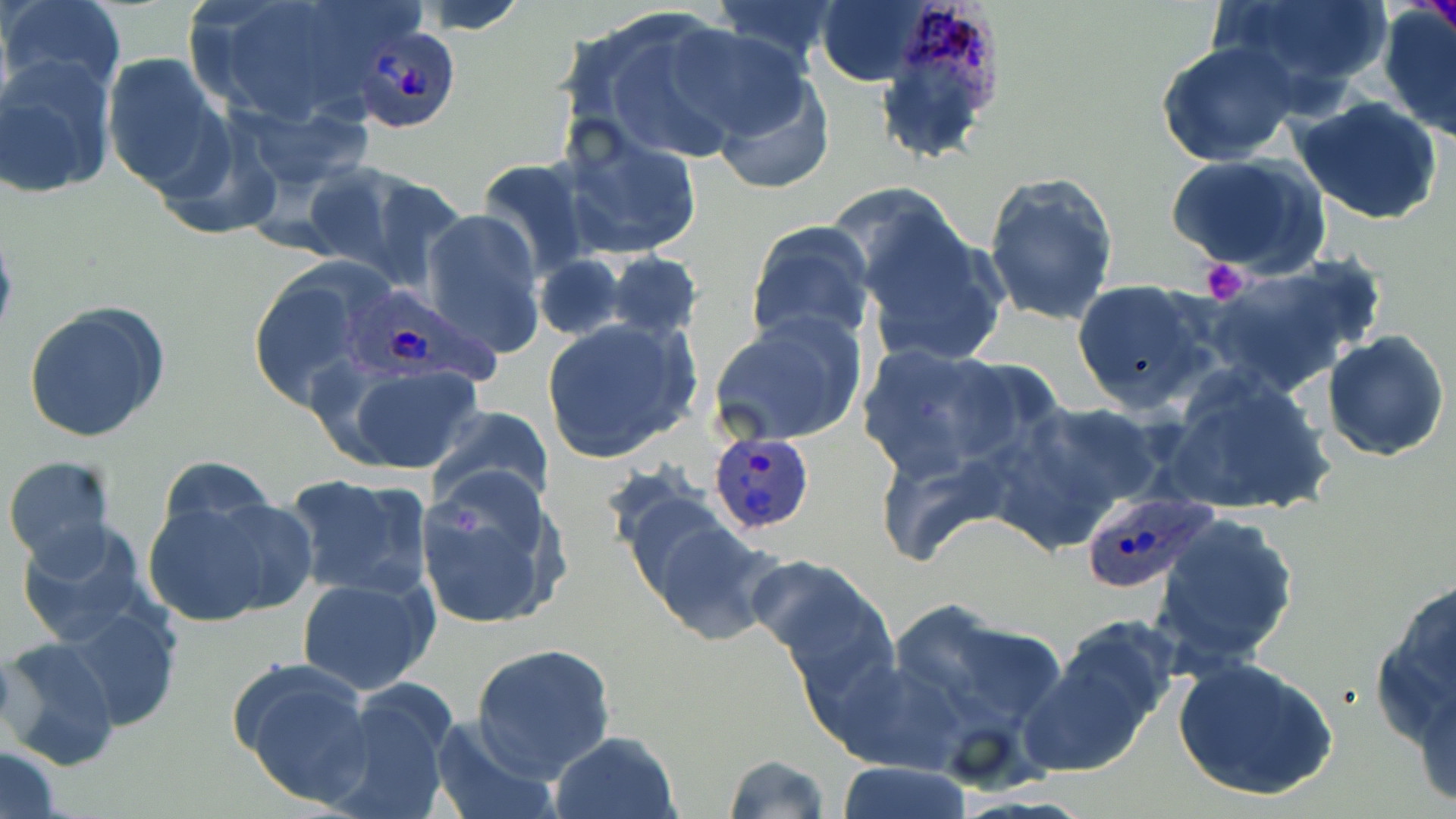

Approximate bounding boxes as (x1, y1, x2, y2) in pixels. Uninfected red blood cell locations: (1, 0, 126, 101), (186, 0, 409, 130), (410, 0, 532, 35), (705, 0, 848, 72), (815, 0, 931, 86), (1207, 0, 1396, 110), (1379, 4, 1456, 137), (570, 10, 750, 164), (663, 23, 819, 147), (1156, 42, 1299, 168), (101, 53, 231, 199), (1, 57, 117, 201), (710, 69, 835, 195), (1290, 95, 1444, 225), (562, 126, 703, 261), (1166, 153, 1327, 279), (475, 160, 596, 282), (303, 162, 457, 288), (982, 171, 1120, 328), (848, 198, 1010, 368), (420, 208, 546, 360), (745, 221, 876, 349), (605, 253, 702, 340), (534, 254, 625, 341), (1199, 254, 1386, 398), (244, 260, 395, 415), (1070, 279, 1219, 415), (22, 301, 170, 444), (709, 313, 870, 445), (542, 316, 701, 464), (1321, 331, 1452, 461), (854, 343, 1022, 480), (334, 361, 487, 476), (1160, 366, 1336, 517), (1013, 401, 1169, 522), (425, 405, 551, 513), (872, 443, 1010, 569), (2, 454, 118, 570), (159, 458, 276, 536), (413, 465, 564, 632), (283, 473, 435, 602), (141, 490, 313, 627), (631, 506, 787, 647), (1151, 511, 1300, 671), (16, 521, 153, 651), (753, 554, 903, 697), (296, 574, 440, 696), (1367, 579, 1456, 750), (896, 602, 1069, 732), (59, 603, 183, 731), (1031, 621, 1176, 769), (3, 637, 123, 770), (471, 643, 617, 780), (1172, 656, 1339, 803), (229, 658, 375, 810), (822, 658, 962, 774), (321, 682, 460, 819), (1411, 684, 1456, 809), (429, 713, 558, 819), (546, 731, 681, 819), (1, 746, 62, 818), (720, 753, 831, 819), (833, 761, 977, 818). Plasmodium ovale-infected red blood cell locations: (893, 0, 1004, 108), (361, 28, 457, 131), (343, 290, 512, 390), (707, 433, 817, 536), (1075, 487, 1220, 596). Platelet locations: (1201, 258, 1250, 305). Slide-level diagnosis: Plasmodium ovale. May-Grünwald-Giemsa stain. Thin blood film. One field of a larger specimen. Optical microscopy. 1000x magnification. Image is 1456×819 pixels.